Locate every Plasmodium falciparum-infected red blood cell.
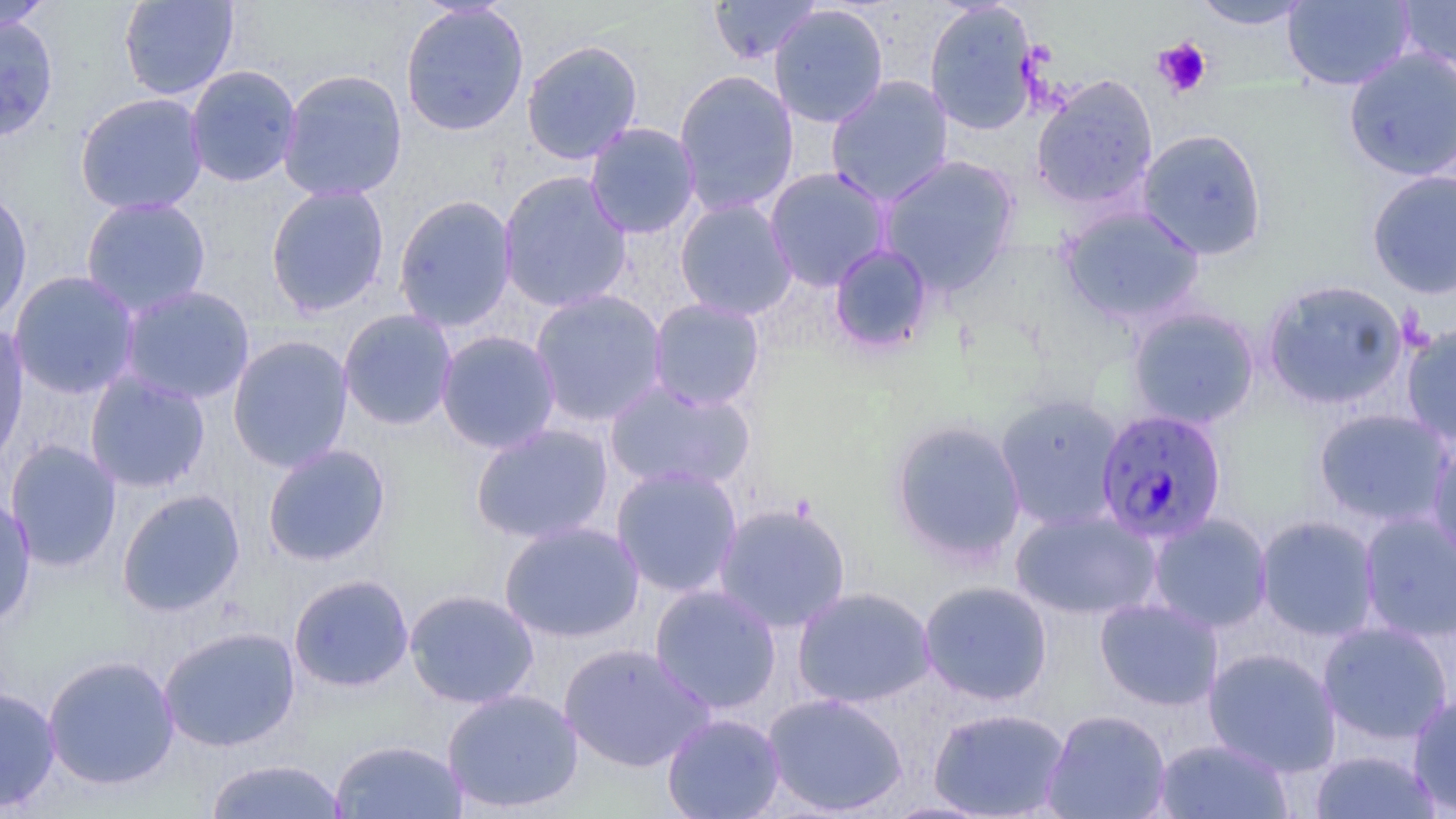
Approximate bounding boxes as (x1,y1)-(x2,y2) corner pairs in pixels.
Plasmodium falciparum-infected red blood cells: (1096,408)-(1228,544).

{
  "slide_level_diagnosis": "Plasmodium falciparum",
  "stain": "May-Grünwald-Giemsa",
  "magnification": "1000x",
  "modality": "optical microscopy",
  "uninfected_red_blood_cell_locations": "approximate bounding boxes as (x1,y1)-(x2,y2) corner pairs in pixels: (0,0)-(55,33), (118,0)-(239,101), (707,0)-(822,65), (1281,0)-(1415,91), (924,1)-(1040,136), (1191,1)-(1314,30), (1396,1)-(1456,75), (400,3)-(530,136), (769,4)-(889,128), (0,13)-(59,143), (521,39)-(644,165), (1342,46)-(1456,181), (184,64)-(303,188), (276,68)-(408,202), (673,69)-(799,217), (1030,74)-(1159,211), (825,75)-(954,207), (74,92)-(209,216), (584,121)-(701,240), (1137,129)-(1268,260), (878,155)-(1020,295), (764,167)-(892,291), (498,170)-(633,313), (1366,170)-(1456,299), (265,184)-(390,317), (0,186)-(34,328), (392,194)-(517,332), (80,196)-(212,318), (674,198)-(798,321), (1058,205)-(1205,325), (828,243)-(935,356), (9,270)-(141,399), (1261,279)-(1409,411), (117,284)-(256,405), (529,288)-(669,428), (648,298)-(766,412), (1127,306)-(1260,429), (338,309)-(458,431), (0,321)-(30,469), (1401,322)-(1456,448), (435,330)-(561,454), (227,335)-(354,473), (84,371)-(211,494), (603,380)-(756,493), (994,393)-(1125,531), (1313,408)-(1455,529), (888,418)-(1027,565), (469,423)-(614,544), (1427,436)-(1456,572), (4,440)-(122,572), (262,443)-(392,567), (611,465)-(743,598), (116,488)-(246,617), (0,492)-(37,630), (713,502)-(852,634), (1010,508)-(1161,620), (1358,511)-(1456,644), (1147,513)-(1273,633), (1255,515)-(1381,641), (498,520)-(645,643), (288,573)-(415,692), (918,580)-(1054,706), (649,584)-(782,715), (792,586)-(936,709), (403,588)-(540,709), (1094,597)-(1224,711), (1317,621)-(1453,745), (158,626)-(301,752), (558,642)-(715,773), (1203,647)-(1342,776), (41,654)-(180,791), (0,685)-(61,813), (441,687)-(585,814), (762,691)-(908,816), (1408,692)-(1456,815), (928,707)-(1071,818), (1042,709)-(1171,818), (661,712)-(785,819), (328,738)-(468,819), (1153,738)-(1294,818), (1309,749)-(1441,818), (203,758)-(349,818)",
  "preparation": "thin blood smear",
  "field_of_view": "one of a larger specimen",
  "platelet_locations": "approximate bounding boxes as (x1,y1)-(x2,y2) corner pairs in pixels: (1153,36)-(1213,98)",
  "image_size": "1456×819 pixels"
}